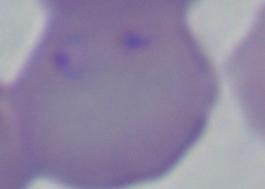

Summary:
  - Identification: Babesia
  - Modality: photomicrograph
  - Magnification: 1000x